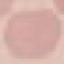
Summary:
  - Result: no malaria parasites seen
  - Capture: smartphone camera at the microscope eyepiece
  - Stain: Giemsa
  - Image type: automatically extracted cell patch, resized to 64 × 64 pixels
  - Preparation: thin smear